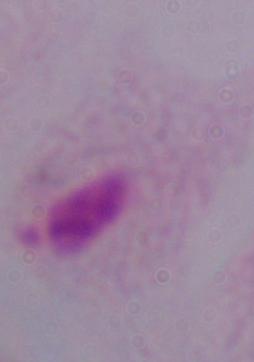

modality = micrograph
magnification = 1000x
identification = trichomonad